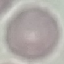
Result: no malaria parasites seen. Thin blood film. Giemsa-stained preparation. Automatically extracted cell patch, resized to 64 × 64 pixels. Acquired by smartphone through the microscope eyepiece.